Give the preparation type.
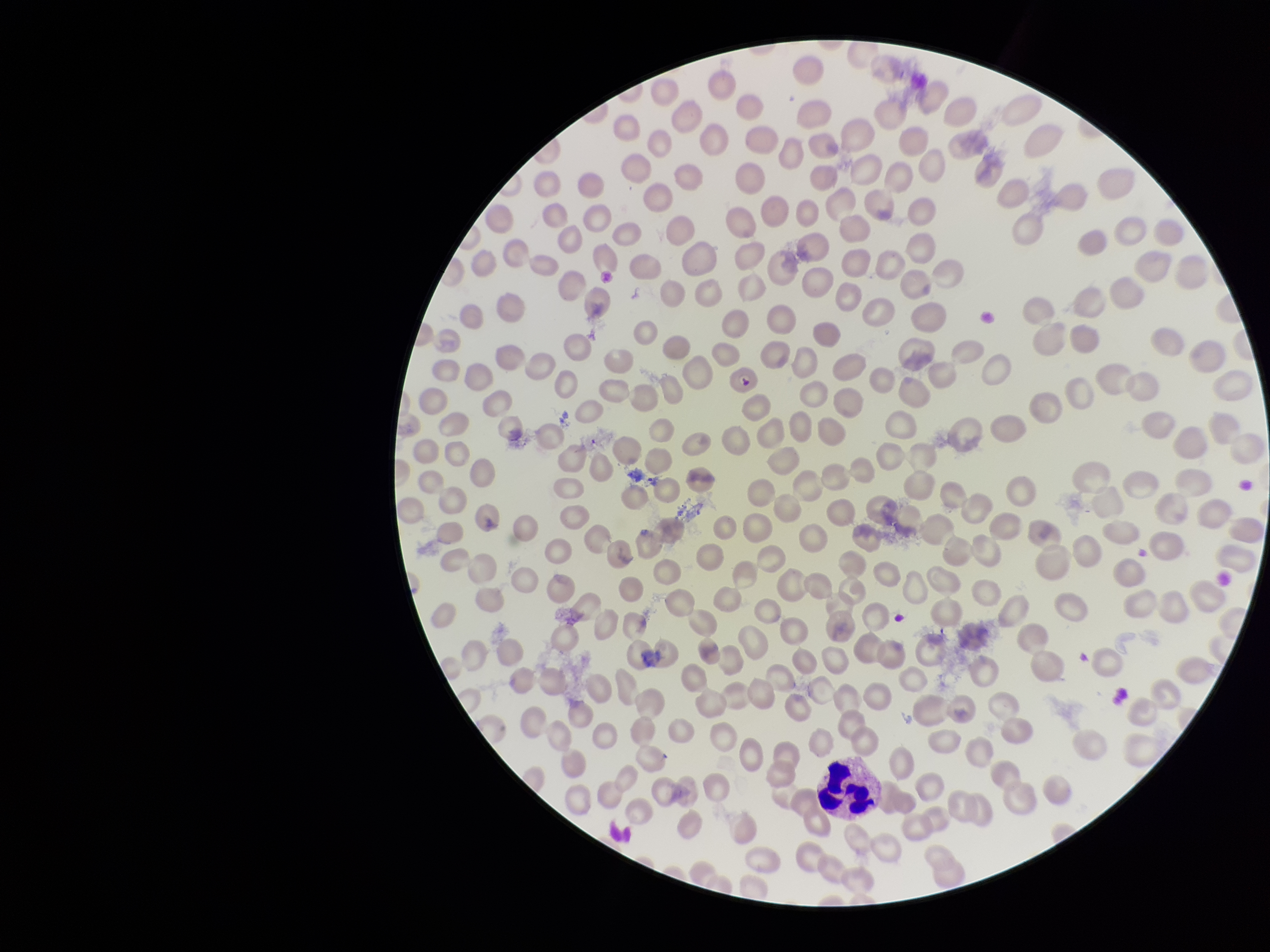
Thin.

Summary:
  - Parasitized red blood cells: none identified
  - Capture: smartphone photograph through the microscope eyepiece
  - Image size: 1270×952 pixels
  - Patient malaria status: infected
  - Stain: Giemsa
  - Species reported for this patient: Plasmodium falciparum
  - Parasitized red blood cell count: 0
  - Red blood cell count: 242
  - Field of view: one from this slide